Report the malaria status of this cell.
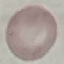

It is uninfected.

image type = cell patch, automatically extracted from a larger field of view and resized to 64 × 64 pixels
preparation = thin blood smear
stain = Giemsa
capture = smartphone through the microscope eyepiece